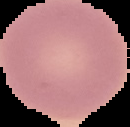
Cell region segmented out of the field of view; the surrounding area is masked to black. Image is 130×127 pixels. From a thin blood smear. Malaria status: uninfected.